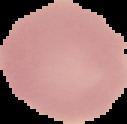

image_size: 127×124 pixels
image_type: segmented cell region on a black background
preparation: thin blood film
result: no malaria parasites seen